Locate every Plasmodium vivax-infected red blood cell.
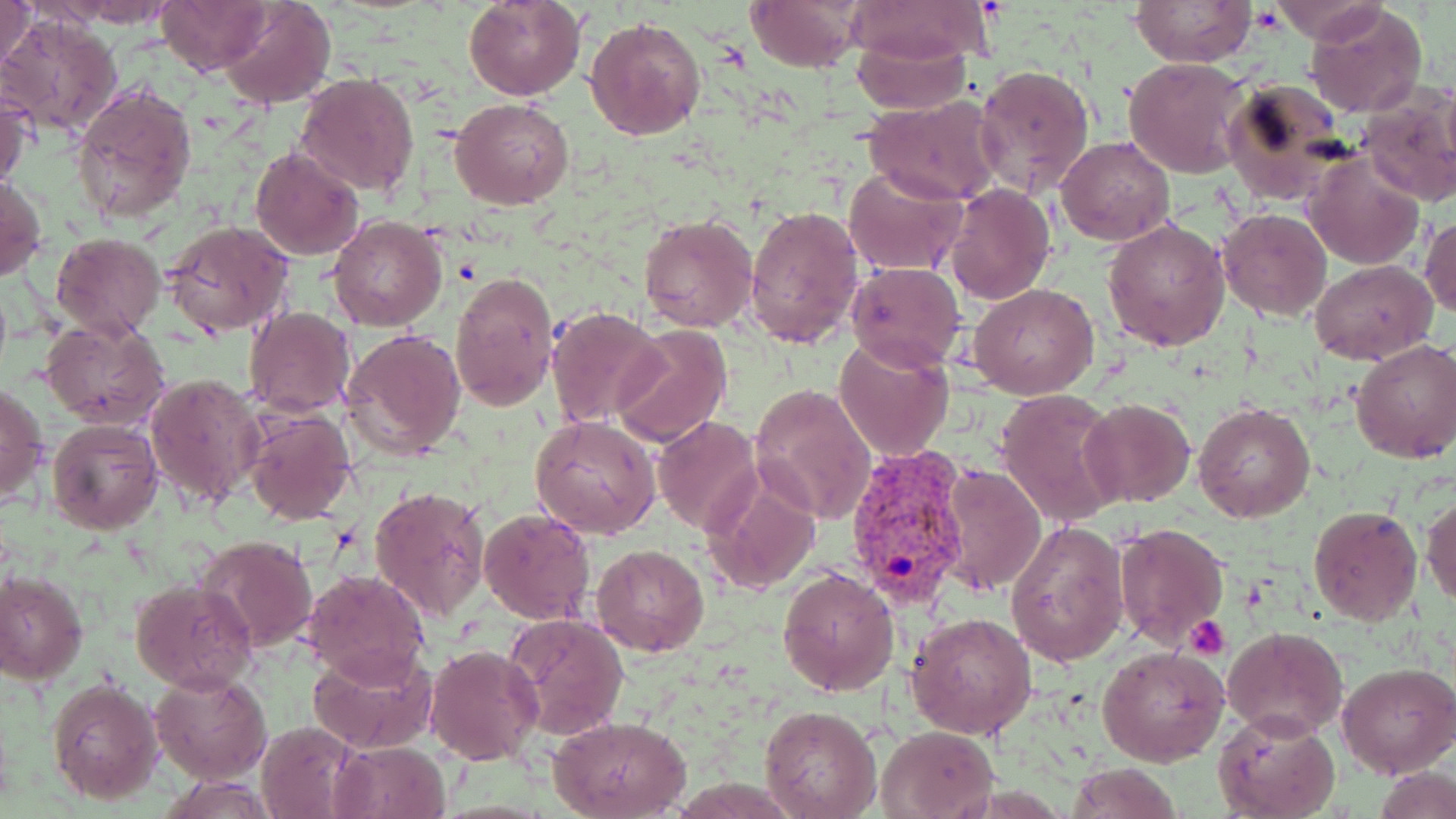
Approximate bounding boxes as named x1/y1/x2/y2 corners in pixels.
Plasmodium vivax-infected red blood cells: (x1=843, y1=446, x2=973, y2=611).

Uninfected red blood cell locations: (x1=1, y1=0, x2=40, y2=74), (x1=61, y1=0, x2=178, y2=26), (x1=156, y1=0, x2=270, y2=75), (x1=219, y1=0, x2=336, y2=110), (x1=465, y1=0, x2=583, y2=100), (x1=744, y1=0, x2=866, y2=72), (x1=843, y1=0, x2=992, y2=66), (x1=1130, y1=0, x2=1254, y2=67), (x1=1265, y1=0, x2=1387, y2=43), (x1=1305, y1=3, x2=1429, y2=118), (x1=3, y1=14, x2=123, y2=139), (x1=585, y1=16, x2=705, y2=140), (x1=853, y1=33, x2=973, y2=113), (x1=1123, y1=57, x2=1250, y2=178), (x1=972, y1=63, x2=1094, y2=197), (x1=296, y1=73, x2=419, y2=195), (x1=1223, y1=74, x2=1350, y2=202), (x1=73, y1=80, x2=197, y2=227), (x1=1358, y1=85, x2=1456, y2=207), (x1=1, y1=90, x2=31, y2=194), (x1=862, y1=96, x2=1002, y2=205), (x1=450, y1=98, x2=575, y2=209), (x1=1057, y1=135, x2=1175, y2=246), (x1=249, y1=146, x2=365, y2=260), (x1=1304, y1=154, x2=1424, y2=271), (x1=843, y1=164, x2=967, y2=277), (x1=0, y1=174, x2=47, y2=282), (x1=943, y1=183, x2=1056, y2=305), (x1=746, y1=203, x2=863, y2=348), (x1=1218, y1=209, x2=1332, y2=322), (x1=639, y1=214, x2=759, y2=333), (x1=1421, y1=214, x2=1455, y2=321), (x1=329, y1=215, x2=446, y2=331), (x1=163, y1=218, x2=296, y2=337), (x1=1104, y1=218, x2=1231, y2=350), (x1=51, y1=233, x2=164, y2=340), (x1=1309, y1=259, x2=1437, y2=363), (x1=846, y1=261, x2=966, y2=369), (x1=450, y1=272, x2=557, y2=410), (x1=970, y1=282, x2=1097, y2=400), (x1=546, y1=306, x2=668, y2=429), (x1=244, y1=307, x2=356, y2=416), (x1=41, y1=318, x2=169, y2=429), (x1=610, y1=323, x2=730, y2=449), (x1=343, y1=328, x2=467, y2=461), (x1=835, y1=338, x2=955, y2=462), (x1=1350, y1=338, x2=1456, y2=464), (x1=146, y1=370, x2=263, y2=509), (x1=1, y1=383, x2=46, y2=504), (x1=748, y1=383, x2=876, y2=526), (x1=996, y1=390, x2=1123, y2=526), (x1=1079, y1=396, x2=1196, y2=508), (x1=1194, y1=400, x2=1315, y2=522), (x1=243, y1=408, x2=357, y2=526), (x1=530, y1=415, x2=659, y2=539), (x1=651, y1=417, x2=761, y2=535), (x1=48, y1=418, x2=161, y2=535), (x1=938, y1=465, x2=1045, y2=594), (x1=701, y1=467, x2=822, y2=596), (x1=369, y1=485, x2=491, y2=621), (x1=1422, y1=494, x2=1455, y2=608), (x1=1308, y1=504, x2=1423, y2=626), (x1=479, y1=507, x2=595, y2=625), (x1=1005, y1=520, x2=1129, y2=667), (x1=1112, y1=521, x2=1228, y2=648), (x1=198, y1=535, x2=317, y2=654), (x1=591, y1=544, x2=708, y2=657), (x1=776, y1=567, x2=901, y2=696), (x1=301, y1=568, x2=430, y2=684), (x1=1, y1=569, x2=87, y2=684), (x1=130, y1=579, x2=256, y2=693), (x1=504, y1=611, x2=631, y2=743), (x1=906, y1=611, x2=1039, y2=741), (x1=1222, y1=626, x2=1348, y2=739), (x1=1097, y1=643, x2=1229, y2=768), (x1=311, y1=644, x2=437, y2=753), (x1=424, y1=645, x2=544, y2=766), (x1=1336, y1=661, x2=1456, y2=778), (x1=151, y1=670, x2=272, y2=784), (x1=46, y1=678, x2=164, y2=805), (x1=760, y1=706, x2=883, y2=819), (x1=1215, y1=708, x2=1340, y2=819), (x1=549, y1=715, x2=689, y2=818), (x1=255, y1=719, x2=361, y2=818), (x1=875, y1=725, x2=996, y2=817), (x1=331, y1=741, x2=450, y2=818), (x1=1064, y1=762, x2=1184, y2=819). Platelet locations: (x1=1185, y1=616, x2=1232, y2=660). Slide-level diagnosis: Plasmodium vivax. Captured at 1000x magnification. May-Grünwald-Giemsa stain. Image is 1456×819 pixels. Single field of view. Thin blood film. Light microscopy.